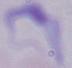

identification = trypanosome
magnification = 1000x
modality = micrograph